Classify this cell by malaria status.
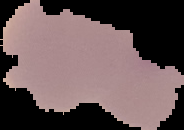

Uninfected.

Summary:
  - Image size: 184×130 pixels
  - Preparation: thin blood smear
  - Image type: segmented cell region on a black background